Locate every malaria parasite and every leukocyte.
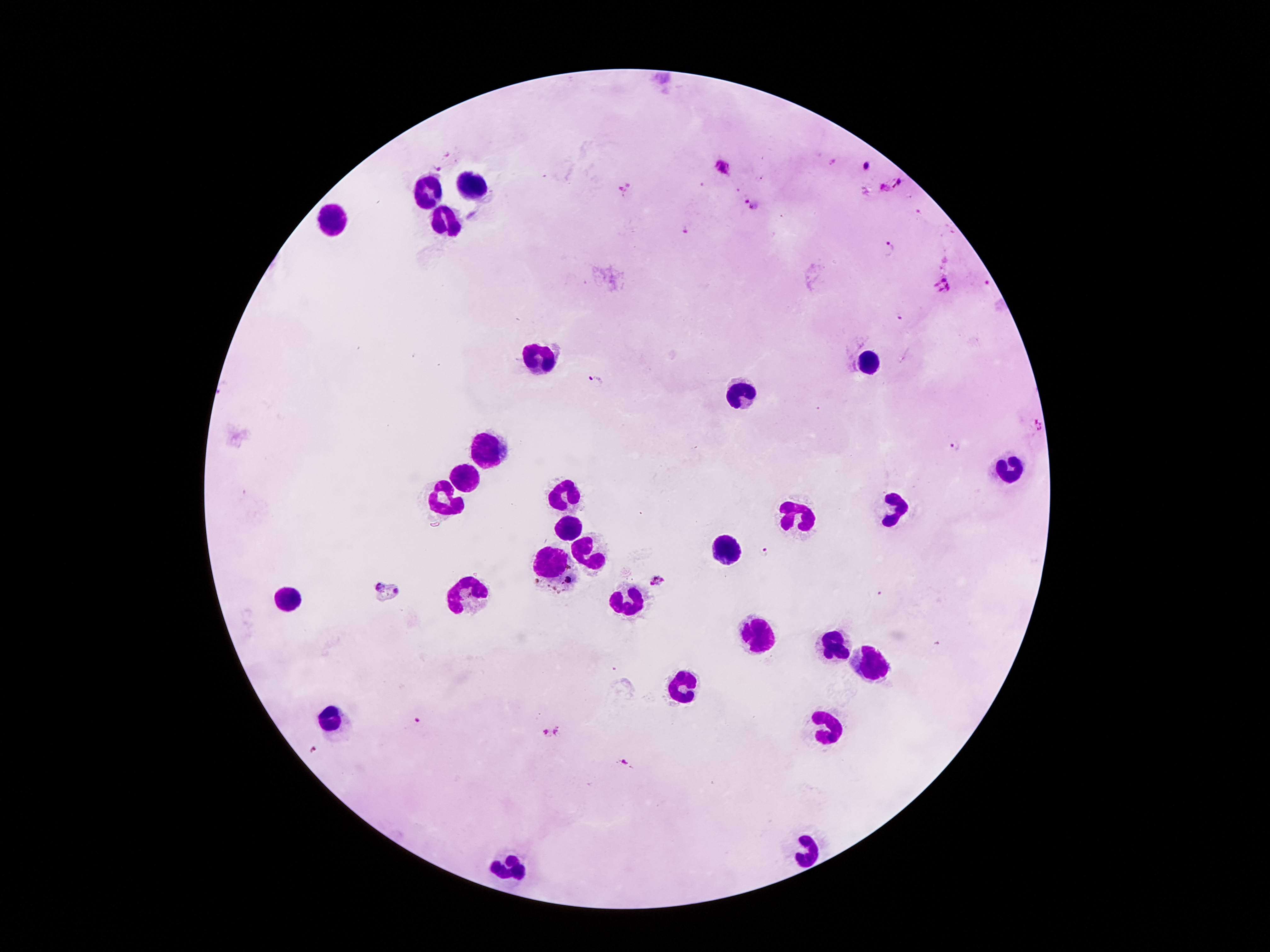

Approximate centers as {x, y} in pixels.
Malaria parasites: {440, 167}, {866, 167}, {721, 168}, {898, 185}, {624, 189}, {748, 204}, {685, 230}, {888, 247}, {986, 281}, {944, 284}, {897, 317}, {596, 379}, {954, 447}, {763, 552}, {658, 582}, {387, 591}, {417, 719}, {551, 734}, {314, 749}, {624, 762}.
Leukocytes: {473, 186}, {425, 189}, {332, 220}, {444, 222}, {542, 359}, {871, 361}, {741, 394}, {484, 449}, {1011, 465}, {464, 483}, {564, 494}, {449, 502}, {893, 507}, {796, 513}, {566, 525}, {730, 547}, {590, 553}, {553, 562}, {467, 593}, {292, 595}, {630, 604}, {759, 631}, {836, 644}, {871, 664}, {681, 684}, {332, 715}, {827, 715}, {807, 851}, {502, 865}.

image size = 1270×952 pixels
magnification = 100x
capture = smartphone through the microscope eyepiece
stain = Giemsa
preparation = thick blood smear
field of view = one from this slide
patient malaria status = positive for Plasmodium falciparum